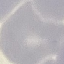

result = no malaria parasites detected
stain = Giemsa
preparation = thin blood smear
capture = smartphone camera at the microscope eyepiece
image type = cell patch, automatically extracted from a larger field of view and resized to 64 × 64 pixels